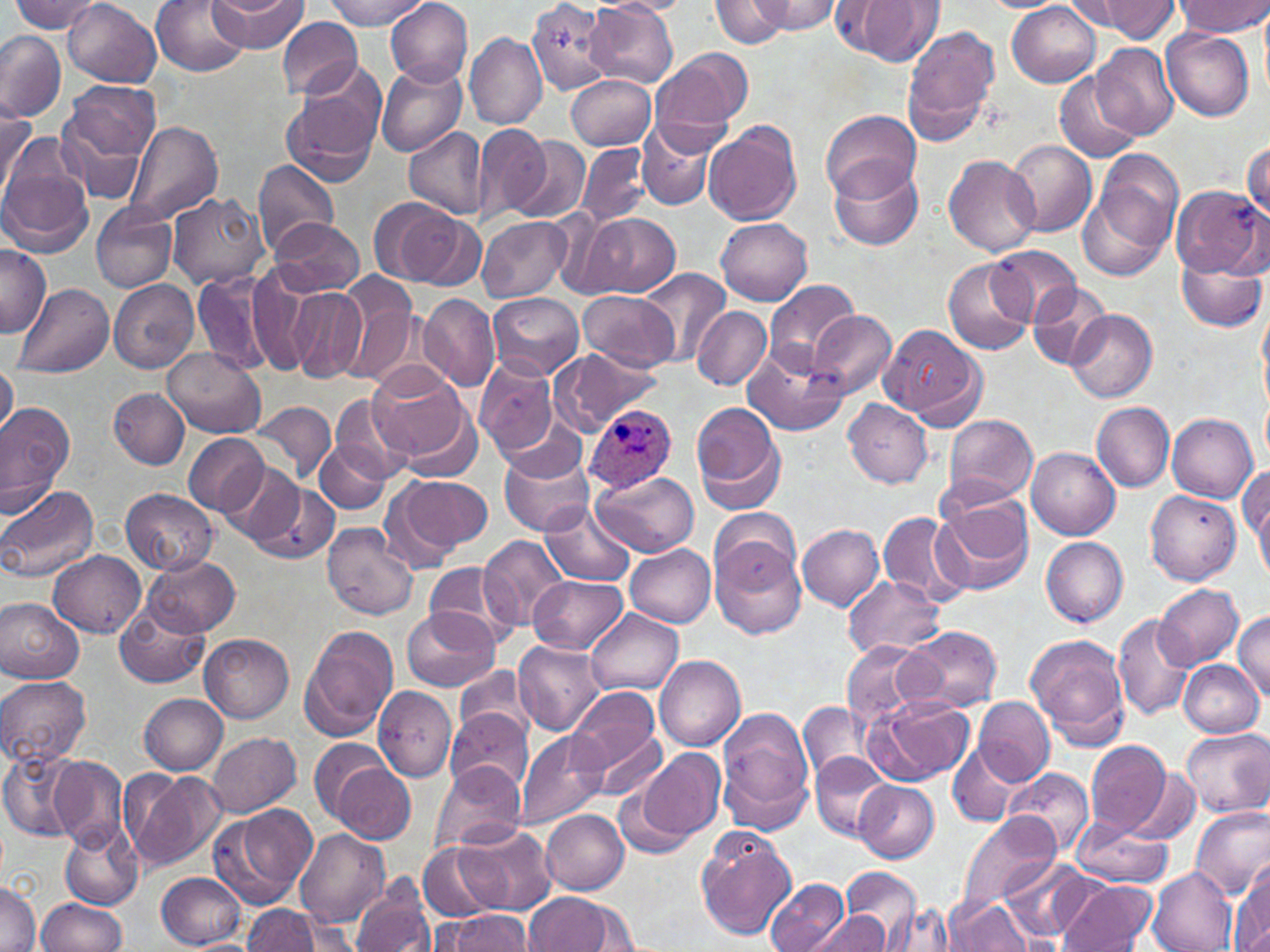

slide-level diagnosis = Plasmodium ovale
stain = May-Grünwald-Giemsa
field of view = single
magnification = 1000x
preparation = thin blood film
Plasmodium ovale-infected red blood cell locations = approximate bounding boxes as named x1/y1/x2/y2 corners in pixels: (x1=585, y1=403, x2=677, y2=494)
modality = optical microscopy
uninfected red blood cell locations = approximate bounding boxes as named x1/y1/x2/y2 corners in pixels: (x1=10, y1=0, x2=103, y2=34), (x1=63, y1=0, x2=162, y2=87), (x1=151, y1=0, x2=250, y2=75), (x1=324, y1=0, x2=426, y2=29), (x1=384, y1=0, x2=473, y2=87), (x1=528, y1=0, x2=615, y2=93), (x1=594, y1=0, x2=691, y2=16), (x1=711, y1=0, x2=793, y2=47), (x1=754, y1=0, x2=840, y2=33), (x1=1060, y1=0, x2=1156, y2=30), (x1=1097, y1=0, x2=1182, y2=41), (x1=207, y1=1, x2=308, y2=53), (x1=585, y1=1, x2=676, y2=87), (x1=839, y1=1, x2=941, y2=65), (x1=1007, y1=1, x2=1101, y2=87), (x1=1175, y1=1, x2=1269, y2=36), (x1=278, y1=16, x2=364, y2=100), (x1=902, y1=24, x2=1000, y2=144), (x1=1161, y1=28, x2=1255, y2=121), (x1=0, y1=32, x2=65, y2=120), (x1=464, y1=32, x2=546, y2=131), (x1=1090, y1=42, x2=1179, y2=141), (x1=649, y1=49, x2=754, y2=144), (x1=376, y1=62, x2=466, y2=158), (x1=283, y1=66, x2=386, y2=182), (x1=1054, y1=73, x2=1142, y2=163), (x1=566, y1=74, x2=656, y2=149), (x1=59, y1=80, x2=159, y2=205), (x1=0, y1=100, x2=34, y2=198), (x1=821, y1=109, x2=919, y2=201), (x1=124, y1=121, x2=224, y2=225), (x1=637, y1=121, x2=721, y2=211), (x1=704, y1=122, x2=803, y2=225), (x1=473, y1=123, x2=554, y2=221), (x1=405, y1=127, x2=488, y2=219), (x1=507, y1=135, x2=591, y2=223), (x1=1007, y1=139, x2=1097, y2=237), (x1=1243, y1=141, x2=1270, y2=220), (x1=576, y1=143, x2=650, y2=227), (x1=0, y1=144, x2=93, y2=258), (x1=1086, y1=150, x2=1185, y2=270), (x1=943, y1=154, x2=1042, y2=257), (x1=828, y1=156, x2=924, y2=252), (x1=253, y1=158, x2=340, y2=257), (x1=1171, y1=185, x2=1266, y2=278), (x1=167, y1=191, x2=271, y2=290), (x1=370, y1=198, x2=477, y2=288), (x1=90, y1=202, x2=177, y2=293), (x1=576, y1=211, x2=682, y2=299), (x1=477, y1=215, x2=571, y2=300), (x1=716, y1=217, x2=812, y2=305), (x1=270, y1=218, x2=368, y2=298), (x1=0, y1=244, x2=51, y2=338), (x1=991, y1=247, x2=1080, y2=325), (x1=1176, y1=254, x2=1265, y2=332), (x1=944, y1=258, x2=1034, y2=356), (x1=240, y1=268, x2=319, y2=374), (x1=639, y1=268, x2=730, y2=366), (x1=193, y1=272, x2=273, y2=377), (x1=334, y1=277, x2=420, y2=385), (x1=107, y1=278, x2=199, y2=374), (x1=764, y1=280, x2=861, y2=373), (x1=1028, y1=280, x2=1114, y2=369), (x1=14, y1=282, x2=114, y2=378), (x1=287, y1=289, x2=366, y2=381), (x1=580, y1=290, x2=678, y2=369), (x1=418, y1=293, x2=501, y2=391), (x1=488, y1=293, x2=584, y2=381), (x1=692, y1=307, x2=771, y2=389), (x1=1065, y1=308, x2=1157, y2=402), (x1=808, y1=310, x2=897, y2=399), (x1=879, y1=324, x2=982, y2=423), (x1=559, y1=347, x2=669, y2=431), (x1=163, y1=348, x2=267, y2=438), (x1=743, y1=350, x2=847, y2=437), (x1=472, y1=358, x2=559, y2=456), (x1=0, y1=362, x2=18, y2=437), (x1=366, y1=364, x2=474, y2=466), (x1=107, y1=386, x2=190, y2=470), (x1=332, y1=393, x2=412, y2=484), (x1=1261, y1=395, x2=1269, y2=466), (x1=843, y1=398, x2=934, y2=487), (x1=692, y1=401, x2=787, y2=513), (x1=254, y1=402, x2=337, y2=485), (x1=1092, y1=402, x2=1173, y2=492), (x1=0, y1=403, x2=75, y2=505), (x1=1166, y1=411, x2=1257, y2=503), (x1=944, y1=412, x2=1040, y2=506), (x1=182, y1=432, x2=270, y2=518), (x1=316, y1=443, x2=391, y2=515), (x1=498, y1=443, x2=595, y2=538), (x1=1027, y1=447, x2=1120, y2=540), (x1=217, y1=462, x2=305, y2=549), (x1=1240, y1=463, x2=1269, y2=560), (x1=592, y1=470, x2=699, y2=558), (x1=382, y1=473, x2=493, y2=568), (x1=249, y1=480, x2=340, y2=565), (x1=1250, y1=481, x2=1270, y2=583), (x1=0, y1=485, x2=101, y2=584), (x1=122, y1=487, x2=217, y2=575), (x1=1145, y1=490, x2=1240, y2=584), (x1=933, y1=493, x2=1034, y2=598), (x1=541, y1=503, x2=634, y2=586), (x1=711, y1=508, x2=800, y2=591), (x1=878, y1=510, x2=969, y2=608), (x1=322, y1=523, x2=418, y2=622), (x1=797, y1=525, x2=885, y2=609), (x1=478, y1=534, x2=569, y2=630), (x1=1040, y1=536, x2=1129, y2=626), (x1=711, y1=538, x2=806, y2=639), (x1=625, y1=542, x2=717, y2=626), (x1=49, y1=551, x2=146, y2=638), (x1=144, y1=555, x2=240, y2=637), (x1=426, y1=562, x2=513, y2=647), (x1=530, y1=575, x2=626, y2=655), (x1=843, y1=575, x2=945, y2=658), (x1=1154, y1=585, x2=1243, y2=670), (x1=0, y1=596, x2=85, y2=684), (x1=116, y1=600, x2=211, y2=688), (x1=403, y1=605, x2=498, y2=691), (x1=585, y1=607, x2=683, y2=695), (x1=1233, y1=610, x2=1270, y2=701), (x1=1113, y1=612, x2=1193, y2=720), (x1=300, y1=625, x2=399, y2=741), (x1=897, y1=626, x2=1004, y2=712), (x1=200, y1=632, x2=294, y2=723), (x1=1026, y1=632, x2=1131, y2=746), (x1=513, y1=640, x2=604, y2=734), (x1=841, y1=641, x2=930, y2=728), (x1=655, y1=654, x2=746, y2=751), (x1=1179, y1=660, x2=1263, y2=736), (x1=455, y1=663, x2=533, y2=741), (x1=0, y1=674, x2=90, y2=767), (x1=374, y1=686, x2=457, y2=782), (x1=566, y1=687, x2=661, y2=778), (x1=140, y1=694, x2=227, y2=774), (x1=867, y1=695, x2=974, y2=785), (x1=974, y1=696, x2=1053, y2=785), (x1=799, y1=701, x2=875, y2=785), (x1=716, y1=706, x2=816, y2=832), (x1=446, y1=707, x2=532, y2=793), (x1=1180, y1=729, x2=1270, y2=816), (x1=591, y1=730, x2=667, y2=801), (x1=207, y1=731, x2=301, y2=817), (x1=513, y1=731, x2=610, y2=830), (x1=1086, y1=739, x2=1176, y2=839), (x1=948, y1=743, x2=1021, y2=827), (x1=637, y1=749, x2=724, y2=843), (x1=1, y1=750, x2=80, y2=844), (x1=323, y1=753, x2=416, y2=844), (x1=810, y1=753, x2=891, y2=842), (x1=51, y1=755, x2=127, y2=848), (x1=431, y1=760, x2=526, y2=854), (x1=1004, y1=766, x2=1094, y2=858), (x1=1123, y1=766, x2=1202, y2=846), (x1=129, y1=771, x2=226, y2=870), (x1=853, y1=779, x2=938, y2=863), (x1=615, y1=784, x2=696, y2=862), (x1=215, y1=805, x2=316, y2=907), (x1=1189, y1=806, x2=1270, y2=901), (x1=540, y1=809, x2=629, y2=894), (x1=957, y1=813, x2=1061, y2=911), (x1=60, y1=822, x2=144, y2=911), (x1=452, y1=823, x2=558, y2=915), (x1=1070, y1=823, x2=1175, y2=887), (x1=294, y1=828, x2=389, y2=929), (x1=696, y1=828, x2=797, y2=941), (x1=418, y1=843, x2=499, y2=921), (x1=1001, y1=856, x2=1092, y2=941), (x1=1231, y1=865, x2=1270, y2=952), (x1=1148, y1=867, x2=1237, y2=952), (x1=843, y1=869, x2=922, y2=944), (x1=156, y1=872, x2=245, y2=949), (x1=764, y1=877, x2=849, y2=952), (x1=350, y1=878, x2=437, y2=952), (x1=0, y1=879, x2=38, y2=952), (x1=1054, y1=879, x2=1158, y2=952), (x1=522, y1=893, x2=624, y2=951), (x1=945, y1=897, x2=1032, y2=951), (x1=36, y1=898, x2=128, y2=952), (x1=243, y1=903, x2=319, y2=951), (x1=885, y1=904, x2=960, y2=952), (x1=439, y1=910, x2=534, y2=950), (x1=811, y1=912, x2=889, y2=952), (x1=191, y1=940, x2=255, y2=952)
image size = 1270×952 pixels